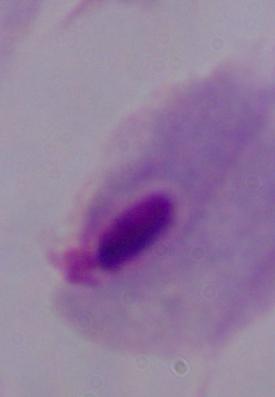 A trichomonad is shown. Micrograph. Captured at 1000x magnification.